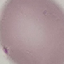 Result: no malaria parasites detected. Cell patch, automatically extracted from a larger field of view and resized to 64 × 64 pixels. Giemsa stain. Thin blood smear. Photographed with a smartphone camera at the microscope eyepiece.